Point out malaria parasites and leukocytes.
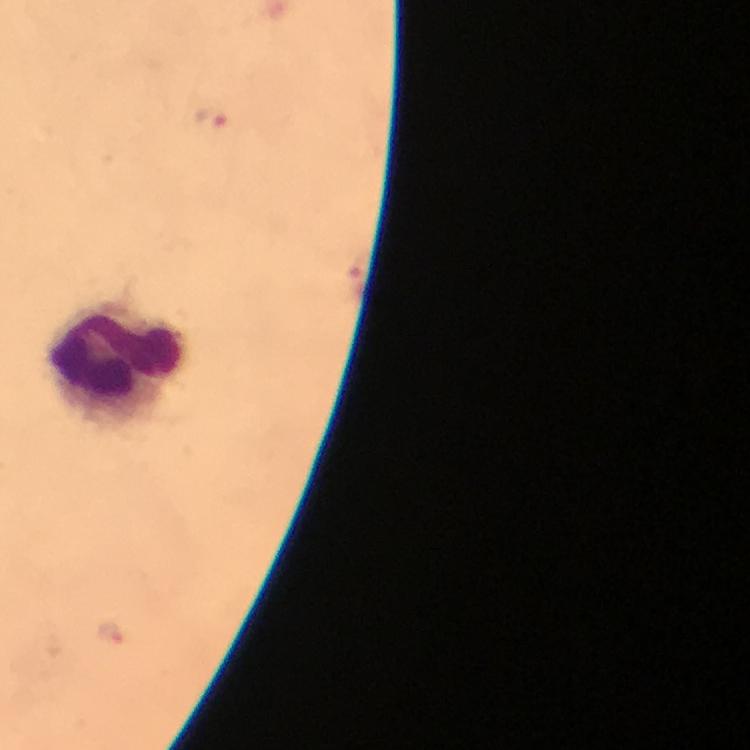

Approximate centers as (x, y) in pixels.
Malaria parasites: (211, 117), (111, 632).
Leukocytes: (115, 365).

{
  "cropped_from": "one field of view",
  "magnification": "100x",
  "stain": "Giemsa",
  "capture": "smartphone photograph through a microscope",
  "image_size": "750×750 pixels",
  "context": "from a diagnostic examination for malaria",
  "immersion_oil": "applied",
  "preparation": "thick smear"
}